Identify the preparation type.
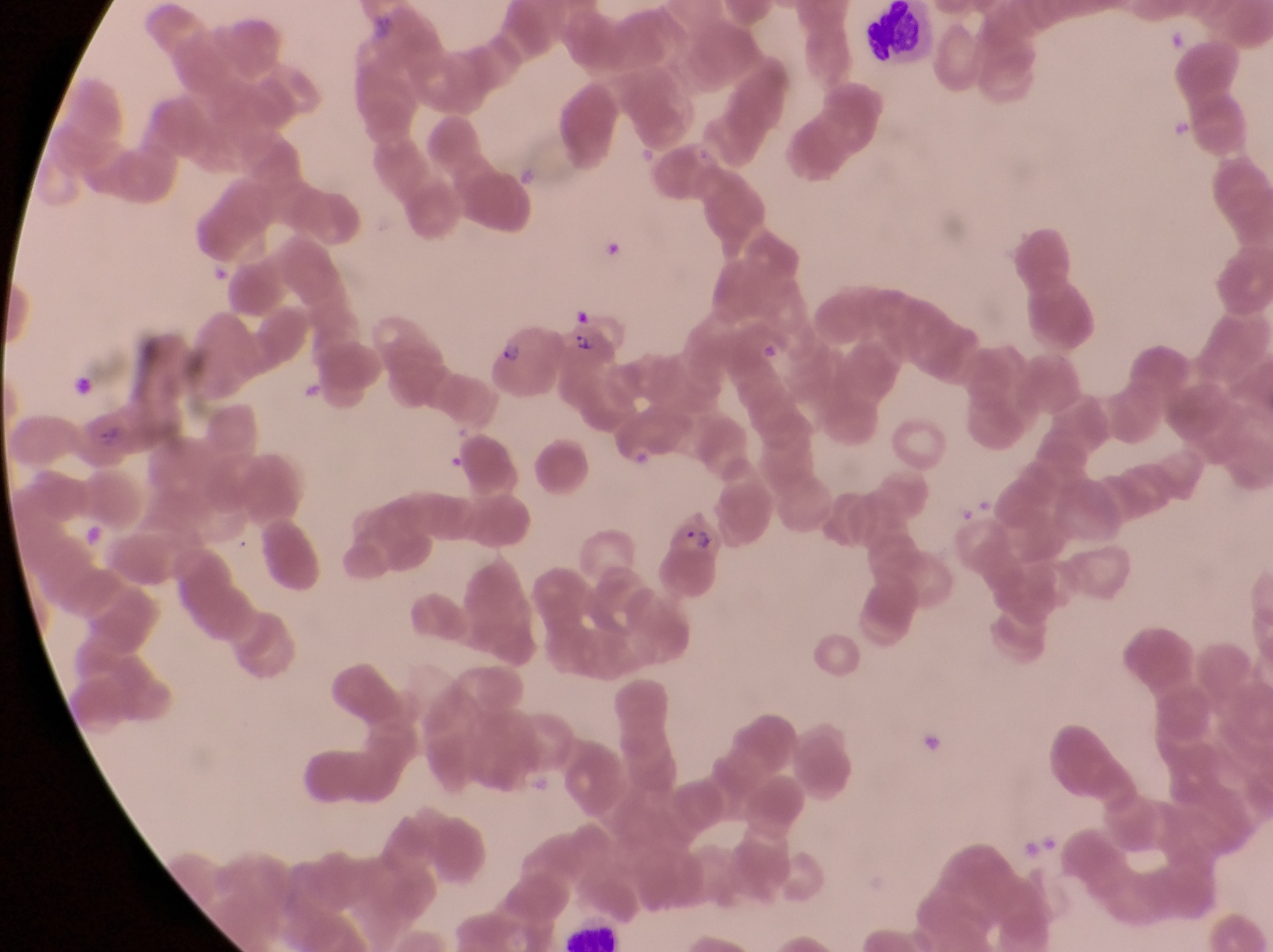
This is a thin smear.

Approximate bounding boxes as {left, top, right, bottom} in pixels.
Summary:
  - Leukocyte locations: {867, 3, 929, 58}
  - Parasitised red blood cell locations: {481, 315, 568, 395}, {565, 315, 623, 410}, {74, 402, 139, 476}, {652, 505, 727, 597}
  - Trophozoite locations: {1166, 112, 1199, 149}
  - Magnification: 1000x
  - Country: Uganda
  - Image size: 1273×952 pixels
  - Capture: smartphone photograph through the eyepiece of an Olympus CX-23 microscope
  - Field of view: single